Identify the parasite.
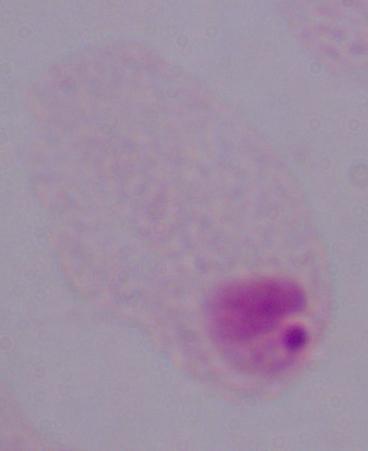

This is a trichomonad.

Summary:
  - Magnification: 1000x
  - Modality: micrograph